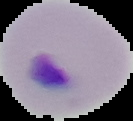 Image is 133×121 pixels. From a thin blood smear. Result: no Plasmodium parasites seen. Segmented cell region on a black background.